State the blood parasite species.
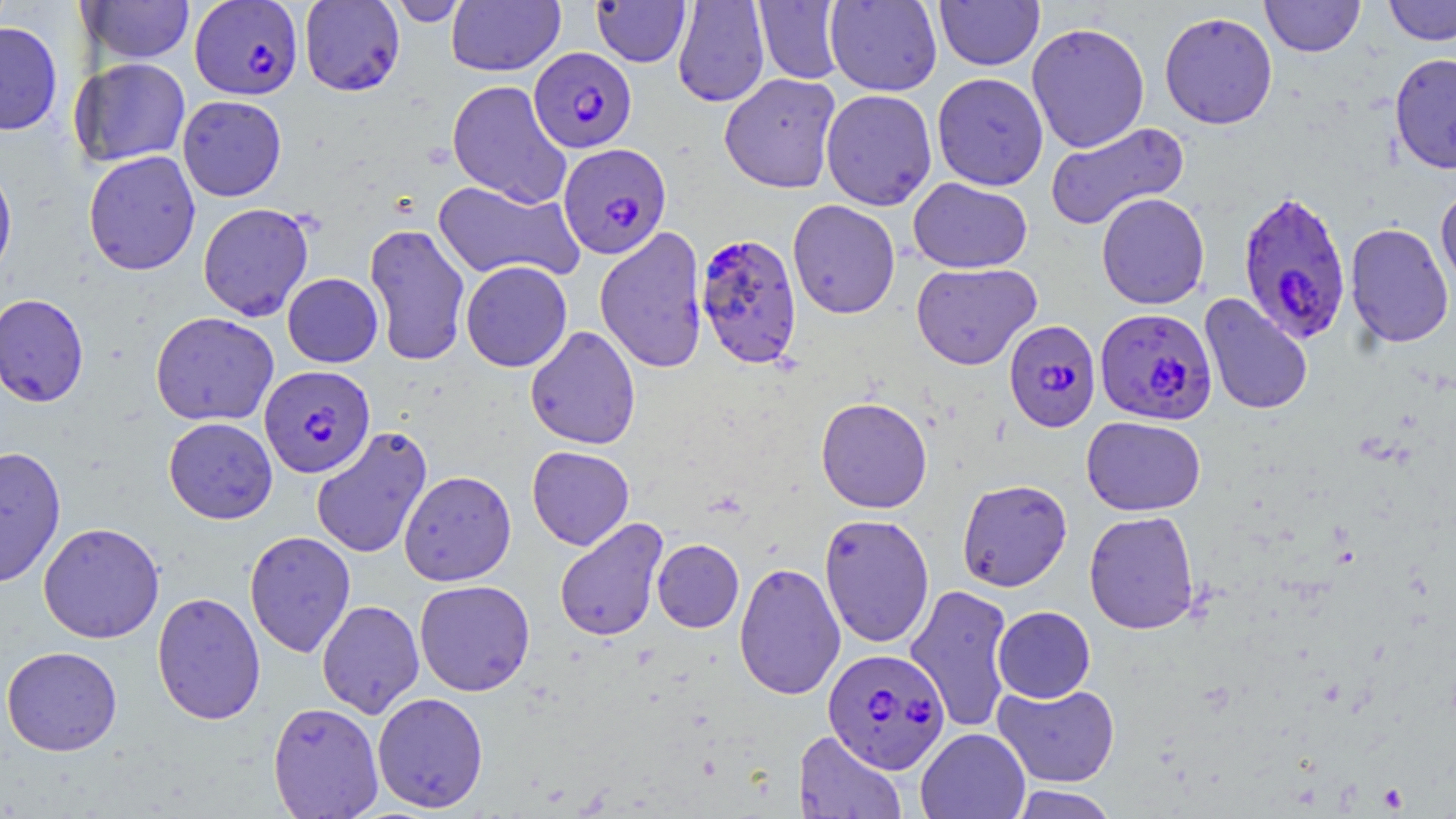

Plasmodium falciparum.

Summary:
  - Coordinate format: approximate bounding boxes as (x1, y1, x2, y2) in pixels
  - Uninfected red blood cell locations: (299, 0, 405, 96), (387, 0, 471, 26), (672, 0, 770, 108), (934, 0, 1045, 71), (1261, 0, 1365, 57), (1384, 0, 1456, 45), (80, 1, 195, 64), (446, 1, 565, 76), (591, 1, 691, 67), (753, 1, 847, 84), (825, 1, 942, 96), (1159, 11, 1278, 129), (0, 21, 63, 135), (1026, 21, 1150, 153), (1389, 51, 1456, 174), (71, 57, 191, 167), (931, 72, 1048, 191), (719, 73, 841, 193), (447, 80, 572, 208), (820, 89, 937, 210), (177, 95, 287, 201), (1044, 121, 1189, 231), (83, 150, 201, 275), (0, 156, 18, 285), (908, 177, 1033, 274), (433, 180, 583, 282), (1435, 184, 1456, 297), (1096, 192, 1210, 310), (787, 199, 900, 319), (197, 202, 314, 321), (1345, 222, 1454, 348), (364, 223, 471, 366), (594, 227, 708, 374), (460, 260, 572, 372), (911, 262, 1042, 370), (282, 273, 383, 367), (0, 293, 89, 407), (1199, 294, 1313, 416), (150, 311, 279, 426), (524, 325, 641, 450), (816, 396, 933, 513), (1081, 415, 1207, 516), (163, 416, 278, 524), (310, 425, 433, 560), (0, 446, 67, 588), (527, 446, 635, 550), (398, 470, 516, 586), (956, 478, 1072, 592), (1083, 510, 1200, 634), (819, 513, 935, 648), (554, 517, 668, 642), (38, 522, 165, 643), (244, 530, 356, 658), (652, 539, 744, 632), (734, 561, 846, 701), (414, 579, 536, 697), (905, 583, 1016, 734), (151, 591, 266, 725), (317, 599, 424, 718), (992, 606, 1095, 703), (1, 646, 122, 755), (992, 683, 1120, 787), (372, 692, 488, 812), (267, 701, 383, 818), (915, 728, 1030, 819), (794, 730, 907, 819), (1008, 785, 1120, 819)
  - Plasmodium falciparum-infected red blood cell locations: (189, 0, 303, 100), (529, 47, 637, 153), (558, 142, 672, 259), (1237, 189, 1352, 345), (695, 232, 803, 369), (1094, 307, 1218, 426), (1004, 319, 1101, 433), (259, 365, 376, 478), (823, 647, 950, 773)
  - Preparation: thin blood smear
  - Modality: optical microscopy
  - Magnification: 1000x
  - Image size: 1456×819 pixels
  - Stain: May-Grünwald-Giemsa
  - Field of view: one of a larger specimen